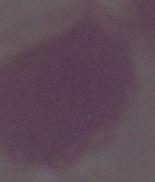

{
  "magnification": "1000x",
  "modality": "micrograph",
  "identification": "red blood cell"
}